Classify this cell by malaria status.
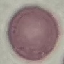

It is uninfected.

Summary:
  - Image type: cell patch, automatically extracted from a larger field of view and resized to 64 × 64 pixels
  - Stain: Giemsa
  - Preparation: thin smear
  - Capture: smartphone camera at the microscope eyepiece